Give the position of every Plasmodium parasite.
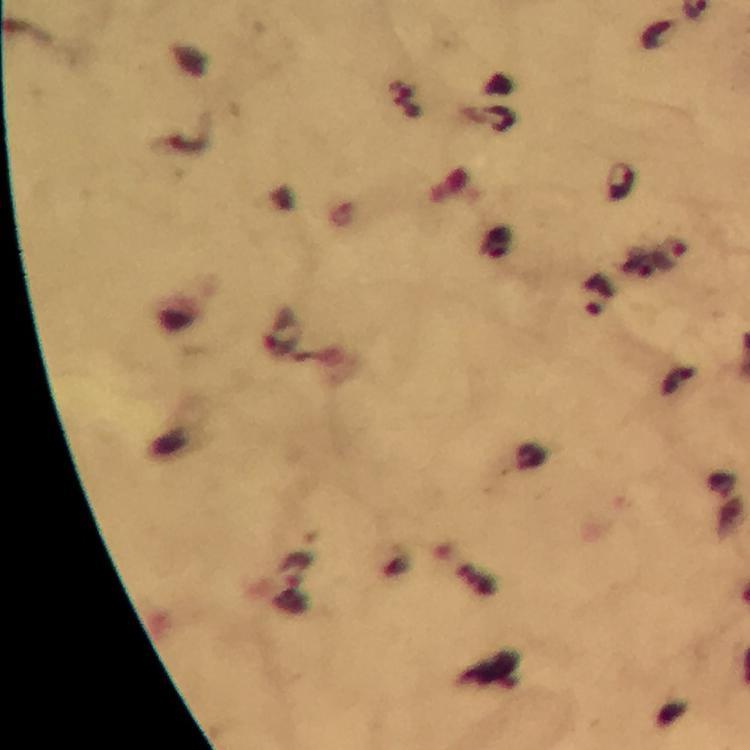

Approximate centers as [x, y] in pixels.
Plasmodium parasites: [621, 182], [670, 253], [598, 295].

Summary:
  - Capture: smartphone camera through the microscope
  - Magnification: 100x
  - Immersion oil: applied
  - Image size: 750×750 pixels
  - Context: from a diagnostic examination for malaria
  - Cropped from: a single field of view
  - Stain: Giemsa
  - Preparation: thick smear